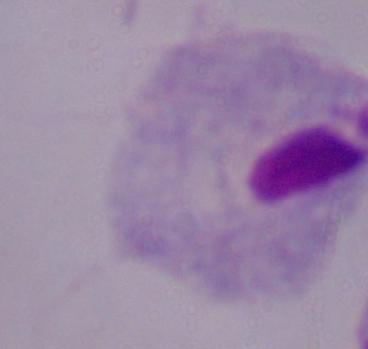
magnification = 1000x
modality = micrograph
identification = trichomonad